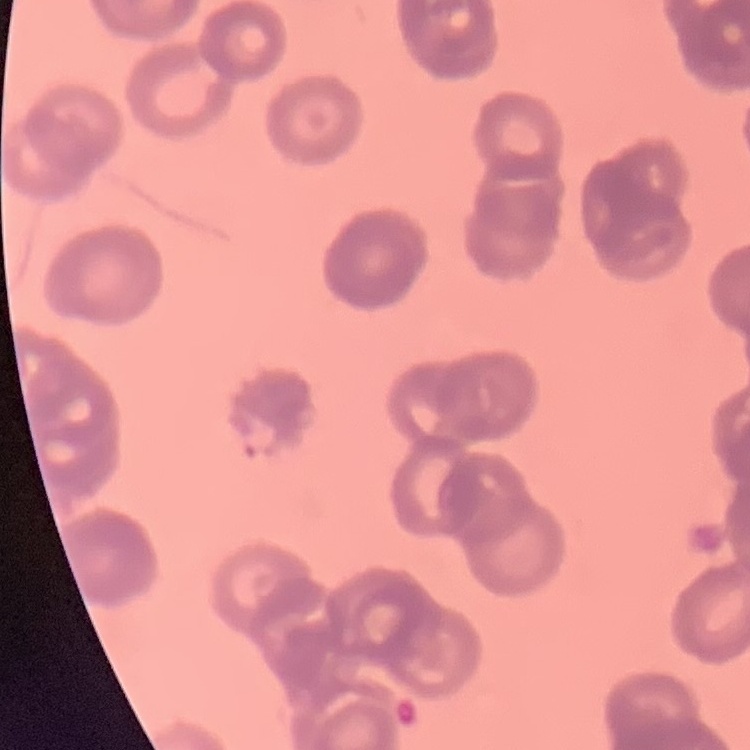
The red blood cells show rouleaux formation. Stained with either Field's or Giemsa. Thin peripheral smear. Square crop of a larger photomicrograph.